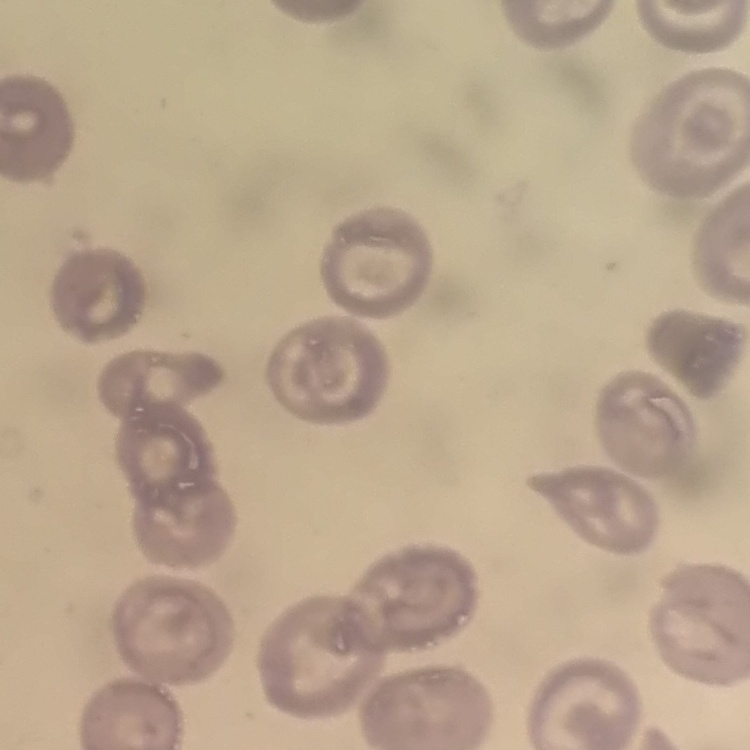

red blood cell morphology = no rouleaux formation
preparation = thin blood smear
stain = Field's or Giemsa
image type = square crop of a larger photomicrograph